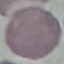
Summary:
  - Malaria status: uninfected
  - Capture: smartphone camera at the microscope eyepiece
  - Stain: Giemsa
  - Image type: automatically extracted cell patch, resized to 64 × 64 pixels
  - Preparation: thin blood smear